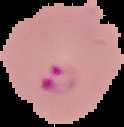
Summary:
  - Image type: segmented cell region on a black background
  - Image size: 124×127 pixels
  - Preparation: thin blood film
  - Malaria status: parasitized